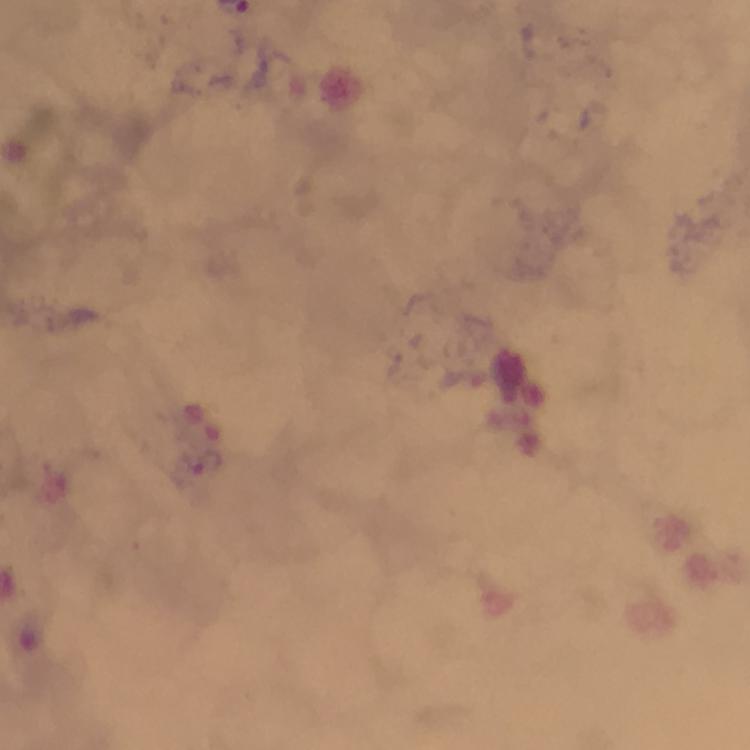

magnification = 100x
immersion oil = applied
cropped from = a single field of view
capture = smartphone photograph through a microscope
context = from a malaria diagnostic workup
preparation = thick smear
image size = 750×750 pixels
stain = Giemsa
malaria parasite locations = approximate centers as {x, y} in pixels: {207, 461}